Report the malaria status of this cell.
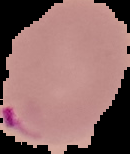
It is parasitized.

image size = 130×154 pixels
preparation = thin blood film
image type = segmented cell region with the area outside set to black